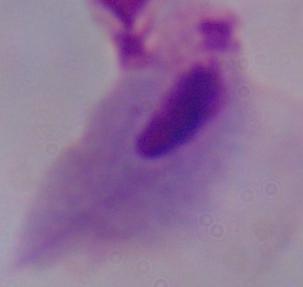

Summary:
  - Modality: micrograph
  - Identification: trichomonad
  - Magnification: 1000x